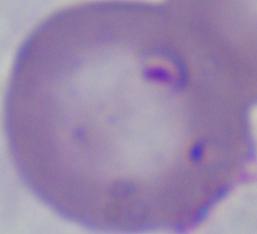
{
  "magnification": "1000x",
  "identification": "Babesia",
  "modality": "micrograph"
}